Comment on the morphology of the red blood cells.
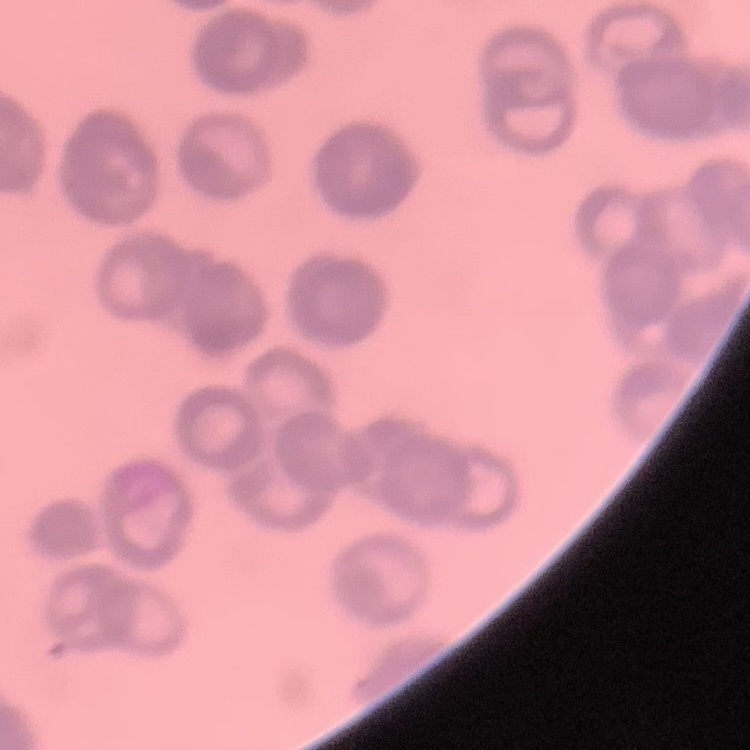
They show rouleaux formation.

Square crop of a larger photomicrograph. Stained with either Field's or Giemsa. Thin peripheral smear.